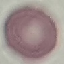

Result: negative for malaria parasites. Photographed with a smartphone camera at the microscope eyepiece. Giemsa stain. Automatically extracted cell patch, resized to 64 × 64 pixels. Thin blood film.